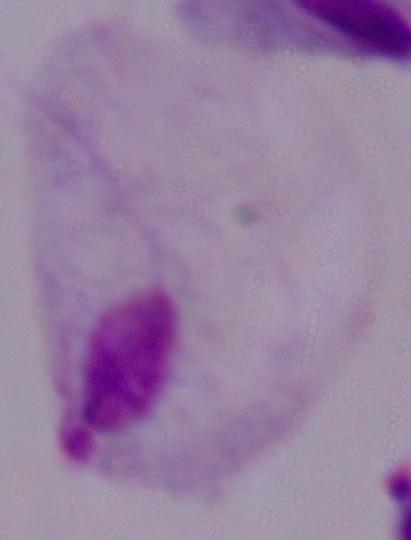

identification = trichomonad
magnification = 1000x
modality = micrograph